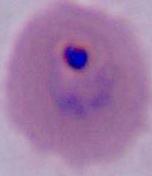

modality = photomicrograph
identification = Plasmodium
magnification = 400x or 1000x